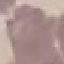
malaria status = uninfected
capture = smartphone camera at the microscope eyepiece
preparation = thin smear
stain = Giemsa
image type = automatically extracted cell patch, resized to 64 × 64 pixels